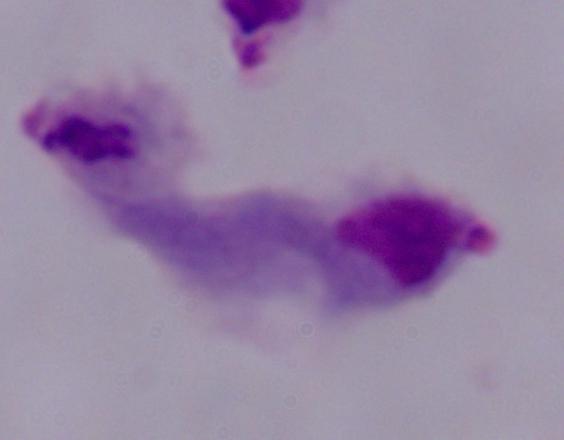

{
  "identification": "trichomonad",
  "modality": "photomicrograph",
  "magnification": "1000x"
}